Give the location of every parasitized red blood cell.
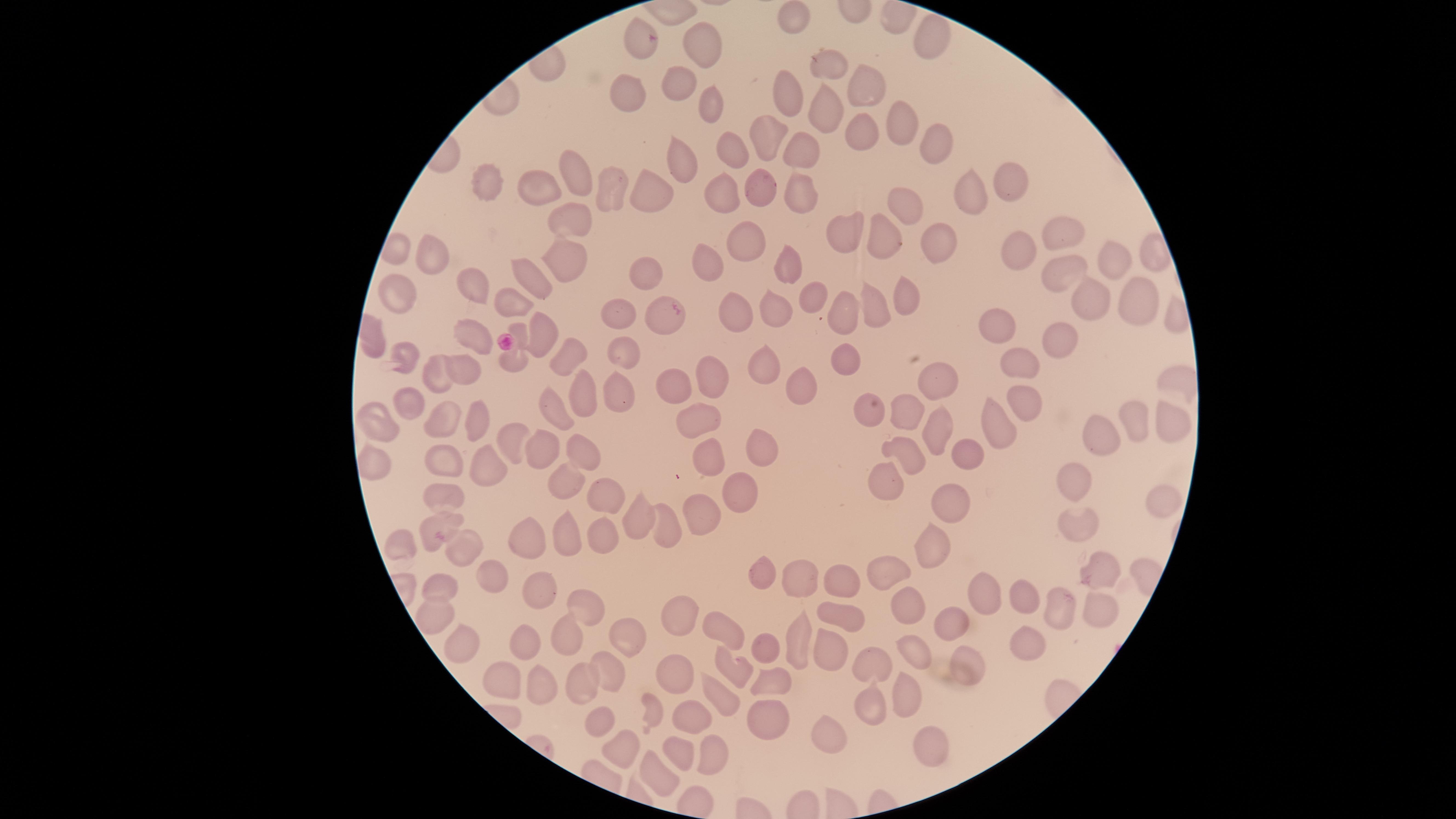
Approximate marker points as {x, y} in pixels.
Parasitized red blood cells: {640, 40}.

capture: smartphone photograph through the microscope eyepiece
field_of_view: single
visible_region: circular
species: Plasmodium falciparum
stain: Giemsa
preparation: thin blood smear
image_size: 1456×819 pixels
uninfected_red_blood_cells: 'approximate marker points as {x, y} in pixels: {795, 16}, {934, 36}, {704, 37}, {821, 67}, {671, 75}, {867, 85}, {782, 87}, {625, 94}, {708, 108}, {816, 111}, {901, 119}, {865, 121}, {762, 135}, {937, 142}, {727, 146}, {799, 153}, {678, 160}, {572, 174}, {485, 180}, {1010, 181}, {537, 185}, {758, 186}, {721, 188}, {609, 194}, {646, 194}, {799, 195}, {968, 195}, {905, 204}, {567, 224}, {1063, 234}, {882, 238}, {943, 240}, {437, 245}, {847, 245}, {740, 247}, {1013, 250}, {562, 259}, {704, 262}, {1114, 262}, {1061, 267}, {792, 269}, {642, 272}, {531, 279}, {473, 284}, {904, 291}, {395, 294}, {810, 296}, {511, 301}, {1091, 301}, {1133, 302}, {876, 305}, {773, 308}, {734, 312}, {843, 313}, {616, 314}, {664, 318}, {996, 323}, {541, 331}, {472, 333}, {1062, 339}, {373, 346}, {511, 353}, {558, 354}, {621, 354}, {840, 358}, {403, 361}, {1022, 361}, {765, 365}, {463, 366}, {432, 371}, {711, 373}, {615, 386}, {672, 386}, {939, 386}, {797, 387}, {406, 399}, {579, 399}, {1023, 399}, {552, 410}, {868, 412}, {699, 414}, {902, 414}, {1164, 414}, {1132, 417}, {448, 420}, {375, 421}, {476, 423}, {995, 423}, {938, 427}, {1097, 432}, {509, 441}, {538, 446}, {583, 450}, {761, 450}, {970, 452}, {714, 455}, {906, 455}, {446, 462}, {378, 466}, {492, 466}, {876, 477}, {1073, 479}, {566, 482}, {439, 493}, {950, 493}, {1160, 495}, {743, 498}, {605, 499}, {700, 512}, {637, 522}, {1072, 522}, {432, 525}, {665, 528}, {525, 535}, {602, 535}, {559, 538}, {398, 545}, {462, 547}, {925, 548}, {1095, 572}, {764, 573}, {489, 578}, {892, 578}, {793, 579}, {845, 582}, {442, 589}, {533, 591}, {981, 596}, {1026, 596}, {903, 601}, {1065, 607}, {581, 608}, {680, 614}, {1100, 615}, {425, 617}, {838, 618}, {951, 620}, {729, 628}, {523, 634}, {618, 637}, {567, 641}, {792, 641}, {1029, 642}, {767, 647}, {826, 647}, {459, 649}, {911, 649}, {966, 658}, {872, 663}, {732, 667}, {602, 673}, {673, 675}, {576, 679}, {770, 681}, {499, 682}, {537, 691}, {909, 694}, {723, 698}, {874, 698}, {654, 705}, {764, 712}, {694, 713}, {596, 723}, {823, 737}, {621, 743}, {927, 743}, {675, 752}, {711, 756}, {653, 771}'